Report the malaria status of this cell.
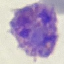
Parasitized.

capture = smartphone camera at the microscope eyepiece
stain = Giemsa
preparation = thin smear
image type = cell patch, automatically extracted from a larger field of view and resized to 64 × 64 pixels